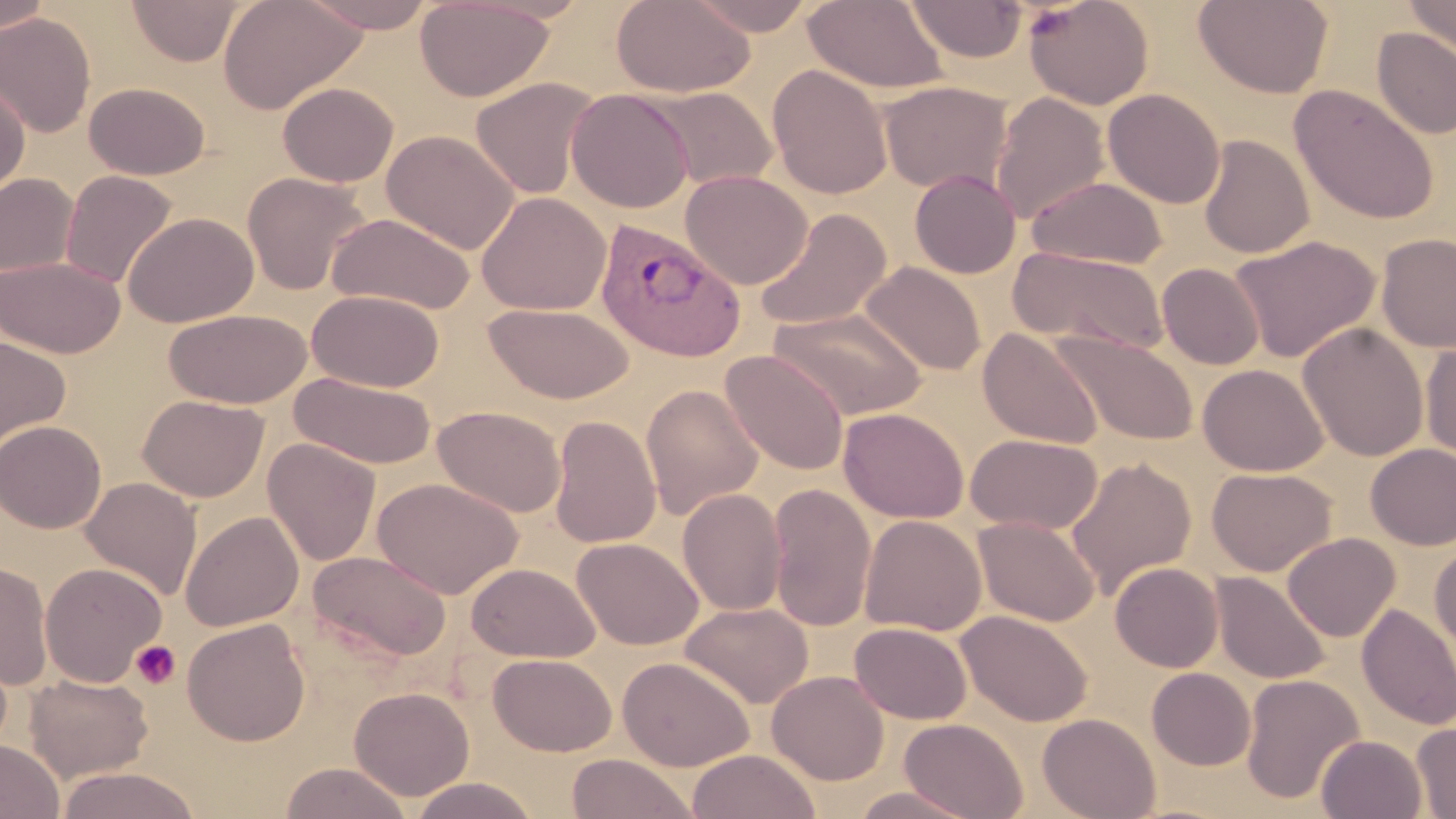

Summary:
  - Coordinate format: approximate bounding boxes as (x1, y1, x2, y2) in pixels
  - Plasmodium vivax-infected red blood cell locations: (596, 220, 747, 363)
  - Platelet locations: (130, 639, 182, 690)
  - Uninfected red blood cell locations: (0, 0, 52, 38), (126, 0, 247, 66), (217, 0, 366, 114), (298, 0, 440, 33), (414, 0, 555, 102), (612, 0, 756, 98), (684, 0, 819, 37), (1024, 0, 1154, 110), (1193, 0, 1333, 99), (1402, 0, 1456, 61), (803, 1, 949, 94), (903, 1, 1027, 63), (0, 11, 97, 137), (1373, 28, 1456, 139), (1336, 37, 1450, 184), (769, 65, 892, 200), (470, 77, 600, 199), (0, 80, 30, 200), (83, 81, 210, 180), (879, 81, 1012, 193), (278, 82, 398, 186), (643, 85, 777, 191), (1289, 85, 1440, 224), (1102, 88, 1225, 209), (566, 89, 694, 213), (990, 92, 1110, 224), (381, 129, 520, 254), (1198, 134, 1314, 259), (681, 169, 812, 289), (909, 169, 1021, 279), (60, 170, 178, 289), (242, 171, 370, 295), (0, 173, 79, 279), (1027, 175, 1168, 269), (476, 192, 611, 316), (754, 208, 892, 329), (326, 211, 476, 314), (123, 212, 259, 327), (1375, 232, 1456, 353), (1229, 234, 1381, 362), (1008, 246, 1169, 354), (0, 256, 125, 358), (860, 262, 987, 376), (1157, 262, 1264, 370), (307, 289, 444, 392), (483, 302, 634, 404), (164, 308, 311, 409), (769, 308, 928, 420), (1297, 324, 1429, 461), (978, 328, 1103, 449), (1051, 330, 1198, 447), (0, 334, 71, 455), (1420, 341, 1456, 464), (720, 350, 849, 476), (1198, 363, 1328, 477), (289, 371, 437, 469), (641, 383, 763, 520), (137, 394, 269, 502), (432, 405, 567, 518), (839, 407, 969, 523), (550, 415, 662, 548), (0, 420, 106, 533), (965, 433, 1103, 534), (263, 438, 381, 566), (1365, 444, 1456, 550), (1066, 457, 1196, 597), (1207, 467, 1336, 576), (80, 477, 202, 601), (372, 477, 523, 599), (767, 482, 877, 633), (677, 488, 787, 616), (180, 510, 304, 632), (859, 514, 987, 637), (973, 516, 1100, 627), (1282, 532, 1400, 641), (572, 536, 703, 650), (1430, 541, 1456, 660), (307, 549, 452, 662), (0, 561, 53, 691), (39, 562, 166, 687), (466, 562, 600, 662), (1110, 562, 1223, 672), (1210, 571, 1331, 685), (680, 601, 813, 709), (1356, 602, 1456, 731), (956, 609, 1092, 727), (182, 618, 310, 746), (849, 621, 972, 724), (488, 653, 616, 756), (618, 656, 755, 771), (1147, 667, 1256, 770), (767, 670, 889, 785), (24, 673, 154, 783), (1241, 673, 1365, 806), (349, 686, 475, 801), (1037, 712, 1161, 819), (898, 718, 1028, 819), (1411, 720, 1456, 817), (1316, 734, 1427, 818), (0, 739, 64, 819), (687, 749, 820, 819), (565, 753, 697, 819), (279, 762, 413, 819), (55, 766, 203, 819), (407, 777, 540, 819), (847, 786, 981, 819)
  - Slide-level diagnosis: Plasmodium vivax
  - Field of view: one of a larger specimen
  - Magnification: 1000x
  - Modality: light microscopy
  - Image size: 1456×819 pixels
  - Stain: May-Grünwald-Giemsa
  - Preparation: thin blood smear